Locate every blood parasite and identify its species.
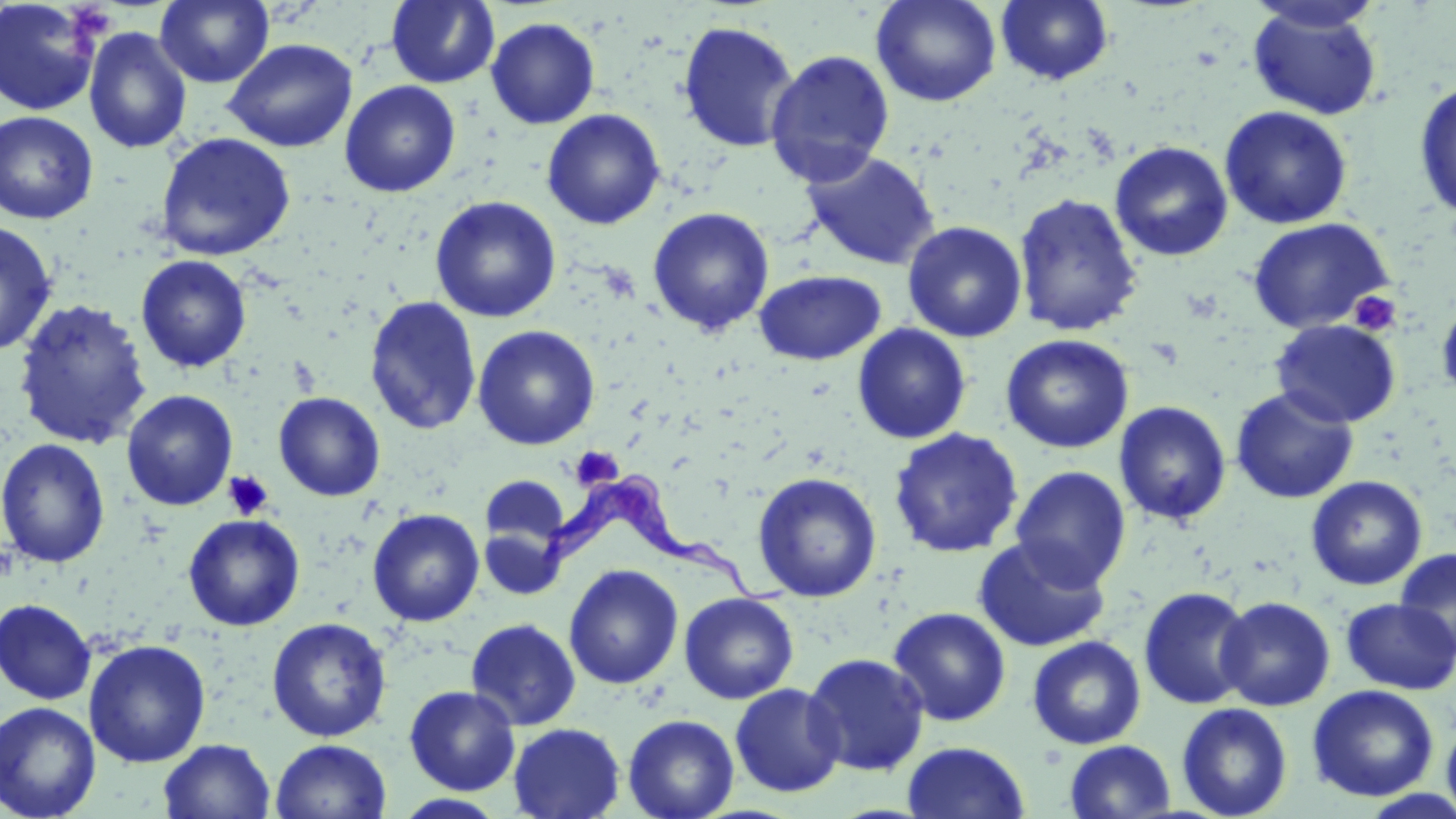

Approximate bounding boxes as [x1, y1, x2, y2] in pixels.
Trypanosoma brucei: [530, 469, 788, 607].
No Plasmodium falciparum, Plasmodium ovale, Plasmodium malariae, Plasmodium vivax, or Babesia divergens observed.

slide-level diagnosis = Trypanosoma brucei
platelet locations = approximate bounding boxes as [x1, y1, x2, y2] in pixels: [1348, 291, 1401, 336], [571, 446, 623, 489], [223, 471, 274, 520]
field of view = single
stain = May-Grünwald-Giemsa
magnification = 1000x
modality = light microscopy
image size = 1456×819 pixels
preparation = thin blood smear
uninfected red blood cell locations = approximate bounding boxes as [x1, y1, x2, y2] in pixels: [1, 0, 103, 116], [154, 0, 274, 88], [386, 0, 500, 88], [870, 0, 1002, 107], [996, 0, 1114, 86], [1245, 1, 1385, 34], [1247, 5, 1383, 121], [485, 17, 600, 129], [676, 20, 800, 153], [83, 27, 192, 154], [222, 38, 358, 153], [764, 49, 895, 187], [1413, 79, 1456, 220], [339, 80, 460, 197], [1219, 105, 1353, 230], [541, 108, 665, 229], [0, 111, 99, 224], [155, 132, 296, 261], [1109, 141, 1234, 262], [800, 151, 941, 270], [1013, 192, 1143, 337], [429, 196, 561, 322], [647, 206, 775, 337], [1247, 218, 1394, 334], [0, 220, 58, 356], [902, 221, 1027, 342], [135, 255, 252, 373], [753, 269, 885, 365], [1436, 294, 1456, 403], [364, 296, 482, 436], [12, 298, 153, 450], [1270, 319, 1401, 428], [852, 323, 972, 444], [472, 325, 600, 450], [1000, 333, 1134, 454], [1231, 386, 1359, 504], [121, 389, 238, 511], [274, 391, 385, 502], [1114, 401, 1231, 526], [888, 427, 1023, 558], [0, 438, 111, 569], [1010, 466, 1131, 590], [752, 471, 882, 602], [481, 474, 570, 549], [1305, 475, 1428, 591], [367, 508, 484, 626], [183, 514, 305, 631], [479, 527, 566, 600], [973, 536, 1112, 653], [1395, 547, 1456, 661], [564, 564, 683, 689], [1138, 586, 1254, 709], [679, 592, 799, 704], [1215, 596, 1335, 711], [0, 598, 97, 704], [1341, 598, 1455, 694], [888, 607, 1011, 727], [266, 617, 392, 742], [465, 618, 581, 730], [1027, 636, 1146, 749], [83, 639, 211, 767], [803, 652, 929, 776], [729, 683, 845, 798], [404, 685, 521, 795], [1307, 685, 1439, 802], [0, 701, 101, 819], [1176, 703, 1293, 818], [623, 714, 739, 819], [1441, 714, 1456, 819], [508, 723, 625, 819], [270, 738, 392, 819], [159, 739, 276, 819], [1065, 740, 1175, 819], [902, 741, 1030, 818], [1357, 790, 1456, 818], [392, 794, 508, 818]